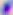

Summary:
  - Modality: photomicrograph
  - Magnification: 400x
  - Identification: Toxoplasma gondii